Name the cell type shown.
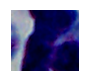

This is a leukocyte.

Summary:
  - Magnification: 1000x
  - Modality: photomicrograph